Report the malaria status of this cell.
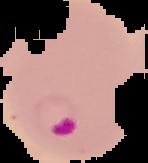
It is parasitized.

Cell region segmented out of the field of view; the surrounding area is masked to black. From a thin blood film. Image is 148×163 pixels.